Classify this cell by malaria status.
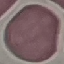
It is uninfected.

capture: smartphone through the microscope eyepiece
stain: Giemsa
image_type: automatically extracted cell patch, resized to 64 × 64 pixels
preparation: thin blood film